Evaluate for malaria.
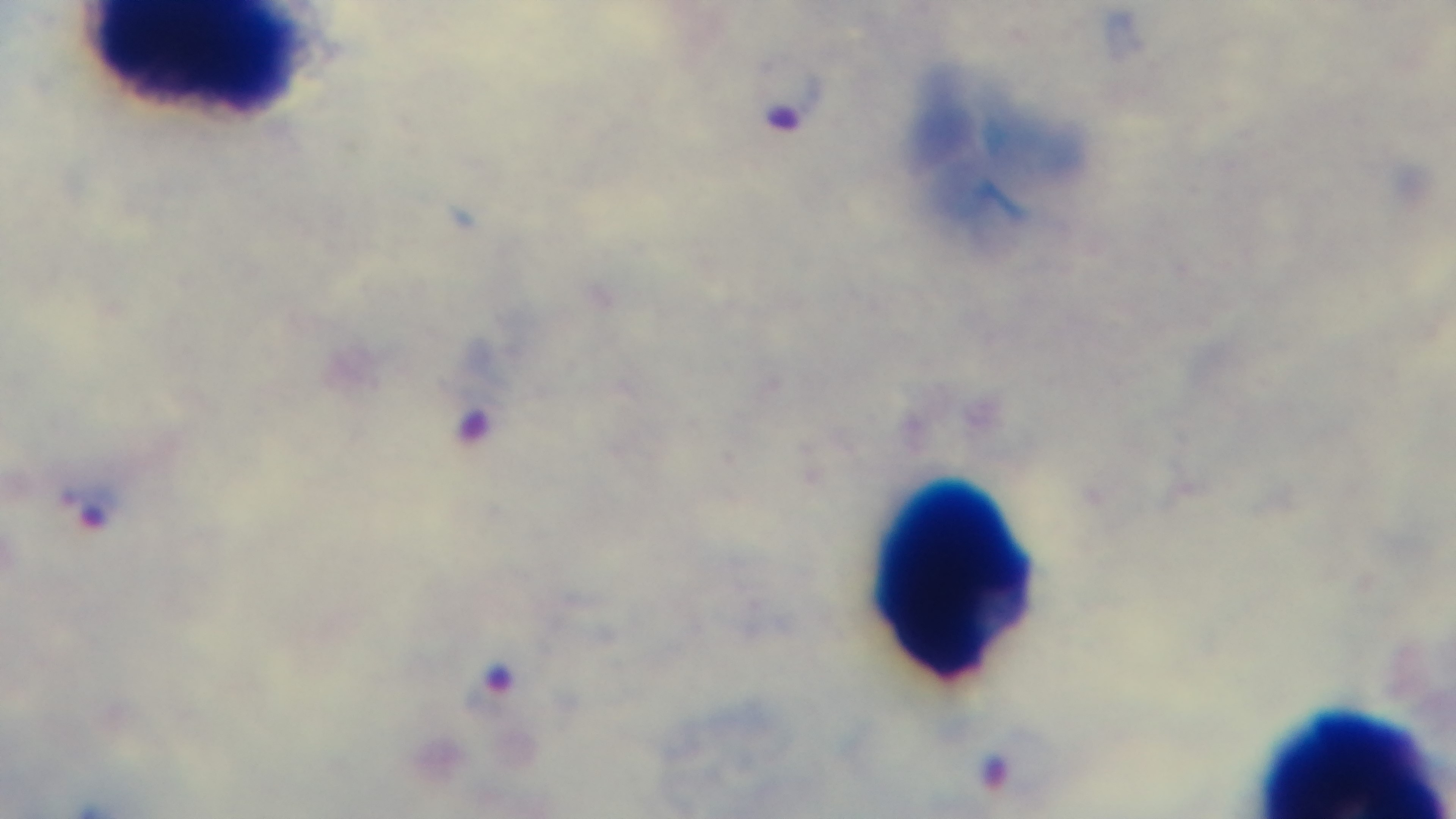

Positive.

stain = Giemsa
modality = light microscopy
objective = 100x oil immersion
field of view = one from the slide
preparation = thick blood film
capture = mounted 4K digital camera